Comment on the morphology of the erythrocytes.
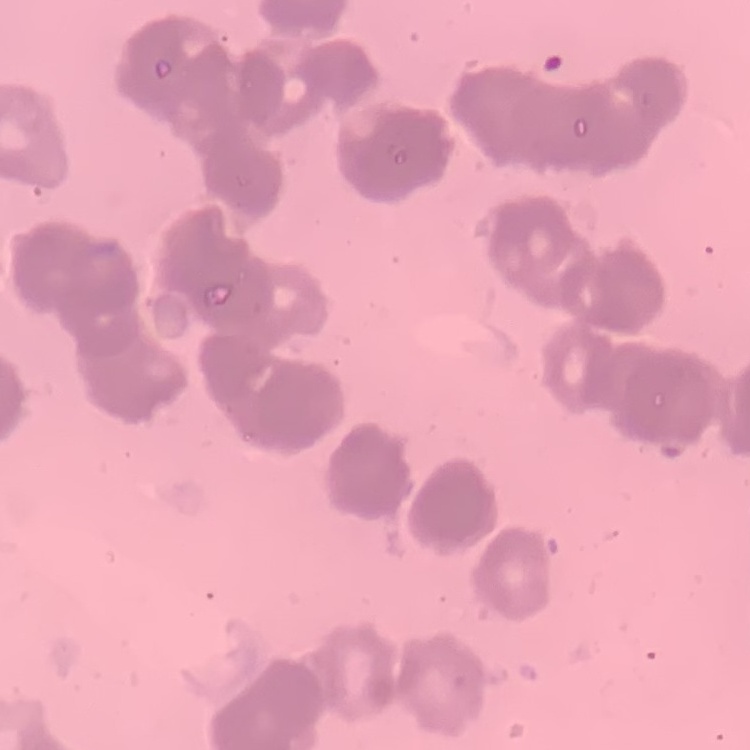
They show rouleaux formation.

Summary:
  - Stain: Field's or Giemsa
  - Preparation: thin peripheral smear
  - Image type: one tile cut from a larger photomicrograph